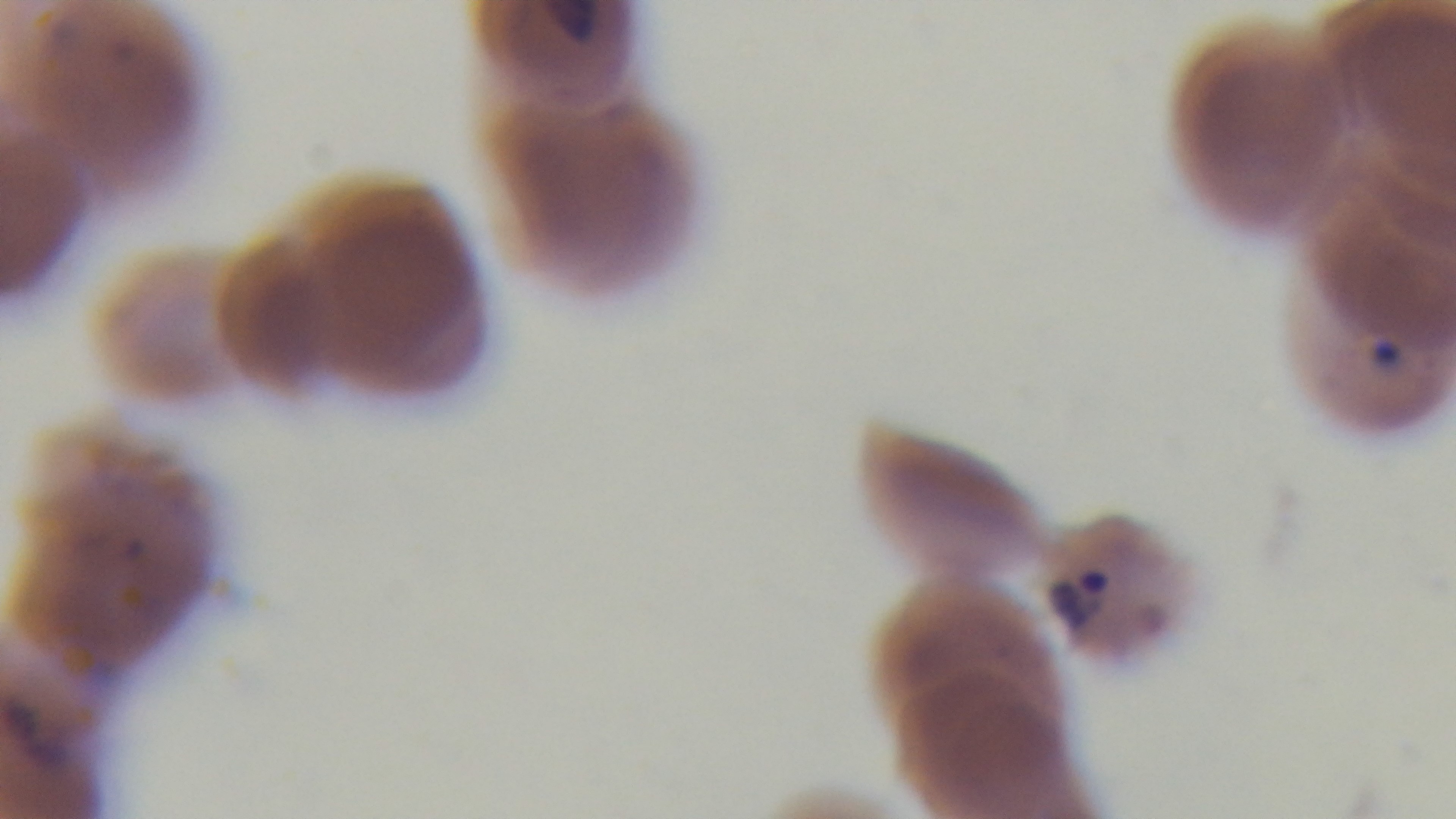

{
  "capture": "mounted 4K digital camera",
  "objective": "100x oil immersion",
  "field_of_view": "single",
  "preparation": "thin blood film",
  "malaria_status": "infected",
  "modality": "light microscopy",
  "stain": "Giemsa"
}